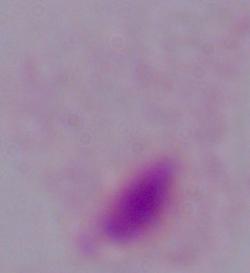
modality: photomicrograph
identification: trichomonad
magnification: 1000x